Report the malaria status of this cell.
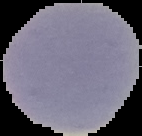

It is uninfected.

image size = 142×136 pixels
preparation = thin blood film
image type = segmented cell region with the area outside set to black